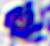

A leukocyte is seen. Micrograph. 400x magnification.